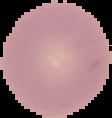
Summary:
  - Image type: segmented cell region on a black background
  - Image size: 112×118 pixels
  - Malaria status: uninfected
  - Preparation: thin blood film